Report the malaria status of this cell.
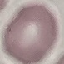

It is uninfected.

Giemsa stain. Cell patch, automatically extracted from a larger field of view and resized to 64 × 64 pixels. Thin smear of blood. Photographed with a smartphone camera at the microscope eyepiece.